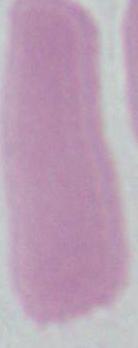

identification = red blood cell
magnification = 1000x
modality = micrograph